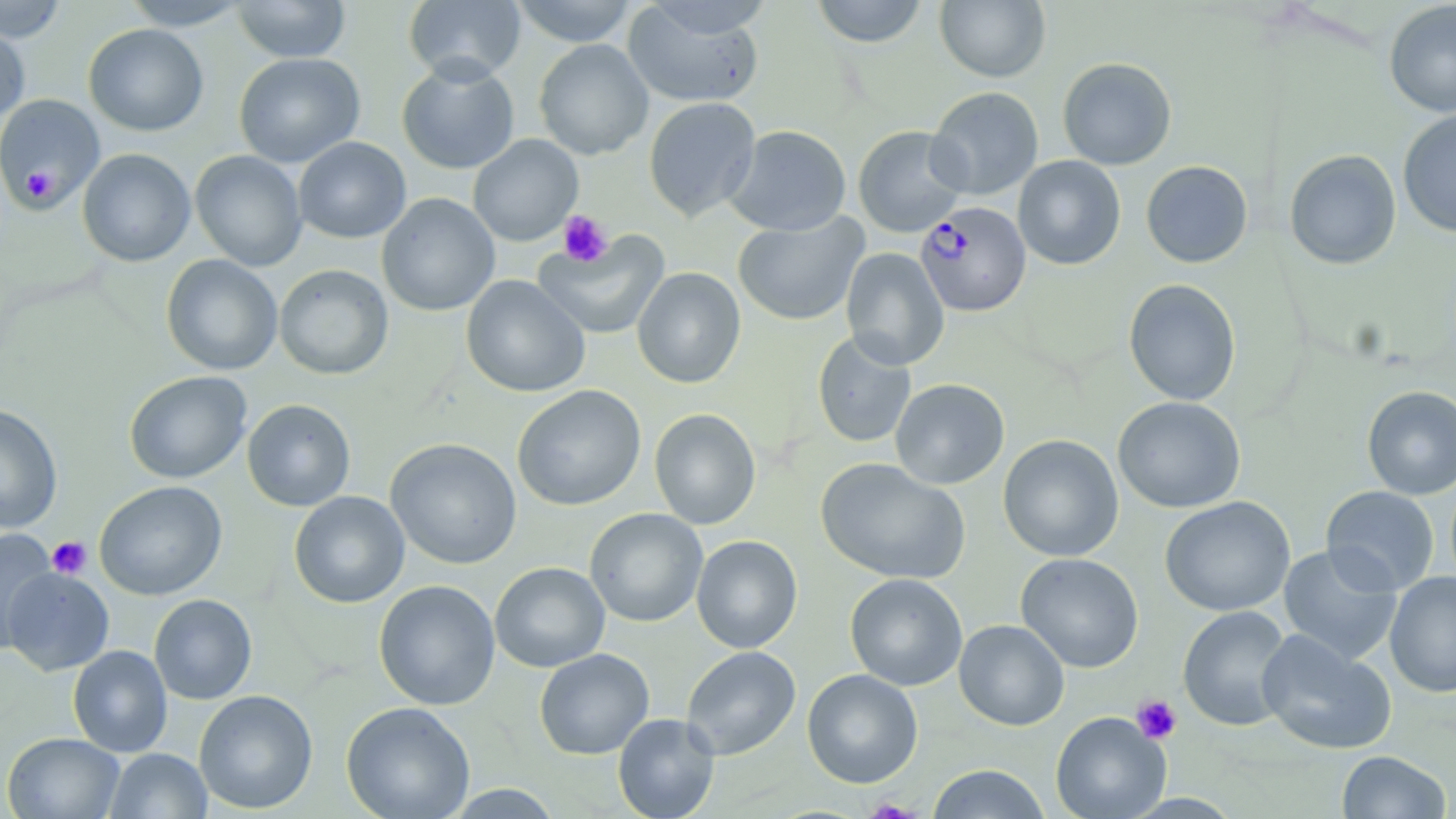

Summary:
  - Coordinate format: approximate bounding boxes as (x1, y1, x2, y2) in pixels
  - Platelet locations: (20, 167, 57, 201), (557, 210, 612, 267), (47, 536, 92, 579), (1131, 694, 1182, 744)
  - Uninfected red blood cell locations: (403, 0, 526, 84), (509, 0, 638, 46), (810, 0, 929, 48), (935, 0, 1051, 83), (0, 1, 68, 43), (120, 1, 252, 30), (232, 1, 351, 62), (622, 1, 767, 109), (1384, 1, 1456, 117), (0, 23, 30, 125), (83, 24, 209, 136), (533, 39, 654, 160), (233, 52, 365, 168), (1058, 57, 1177, 170), (397, 59, 520, 174), (926, 86, 1044, 200), (0, 94, 105, 213), (643, 96, 761, 222), (1397, 108, 1456, 238), (724, 124, 852, 236), (853, 125, 970, 238), (468, 134, 583, 246), (293, 137, 411, 243), (77, 148, 196, 267), (1284, 149, 1402, 270), (189, 150, 308, 271), (1013, 155, 1126, 270), (1141, 160, 1253, 268), (376, 193, 500, 316), (732, 213, 869, 326), (533, 231, 670, 340), (840, 247, 949, 370), (161, 254, 283, 376), (274, 264, 393, 380), (632, 267, 746, 388), (461, 275, 591, 398), (1123, 278, 1241, 405), (811, 331, 917, 448), (124, 371, 252, 484), (890, 378, 1010, 489), (512, 385, 646, 510), (1362, 386, 1456, 499), (1112, 396, 1246, 514), (242, 399, 356, 511), (0, 404, 63, 534), (648, 408, 761, 530), (998, 434, 1124, 562), (385, 438, 522, 569), (816, 458, 970, 585), (94, 481, 228, 601), (1320, 486, 1440, 595), (289, 490, 410, 608), (1159, 496, 1296, 616), (584, 508, 708, 627), (0, 528, 59, 652), (691, 535, 803, 653), (1277, 544, 1403, 666), (1015, 552, 1144, 672), (489, 562, 610, 672), (2, 568, 114, 675), (1385, 571, 1456, 698), (844, 573, 967, 691), (373, 579, 500, 710), (149, 594, 257, 704), (1177, 605, 1294, 731), (954, 619, 1070, 731), (1256, 630, 1397, 756), (68, 645, 172, 757), (680, 646, 801, 760), (534, 648, 655, 760), (802, 669, 923, 788), (194, 690, 318, 814), (340, 701, 475, 819), (1050, 711, 1171, 819), (612, 713, 721, 819), (2, 732, 124, 818), (105, 748, 212, 818), (1337, 750, 1452, 818), (926, 764, 1052, 818), (445, 784, 563, 818)
  - Plasmodium falciparum-infected red blood cell locations: (915, 201, 1031, 316)
  - Slide-level diagnosis: Plasmodium falciparum
  - Stain: May-Grünwald-Giemsa
  - Image size: 1456×819 pixels
  - Preparation: thin blood smear
  - Magnification: 1000x
  - Modality: light microscopy
  - Field of view: single